Assess this cell for malaria.
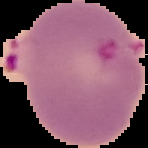
Parasitized.

From a thin blood smear. The area outside the segmented cell region is set to black. Image is 148×148 pixels.